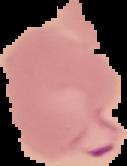

Malaria status: parasitized. Image is 127×166 pixels. Segmented cell region on a black background. From a thin blood smear.